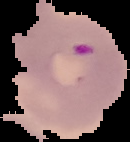
The area outside the segmented cell region is set to black. From a thin blood smear. Malaria status: parasitized. Image is 130×142 pixels.